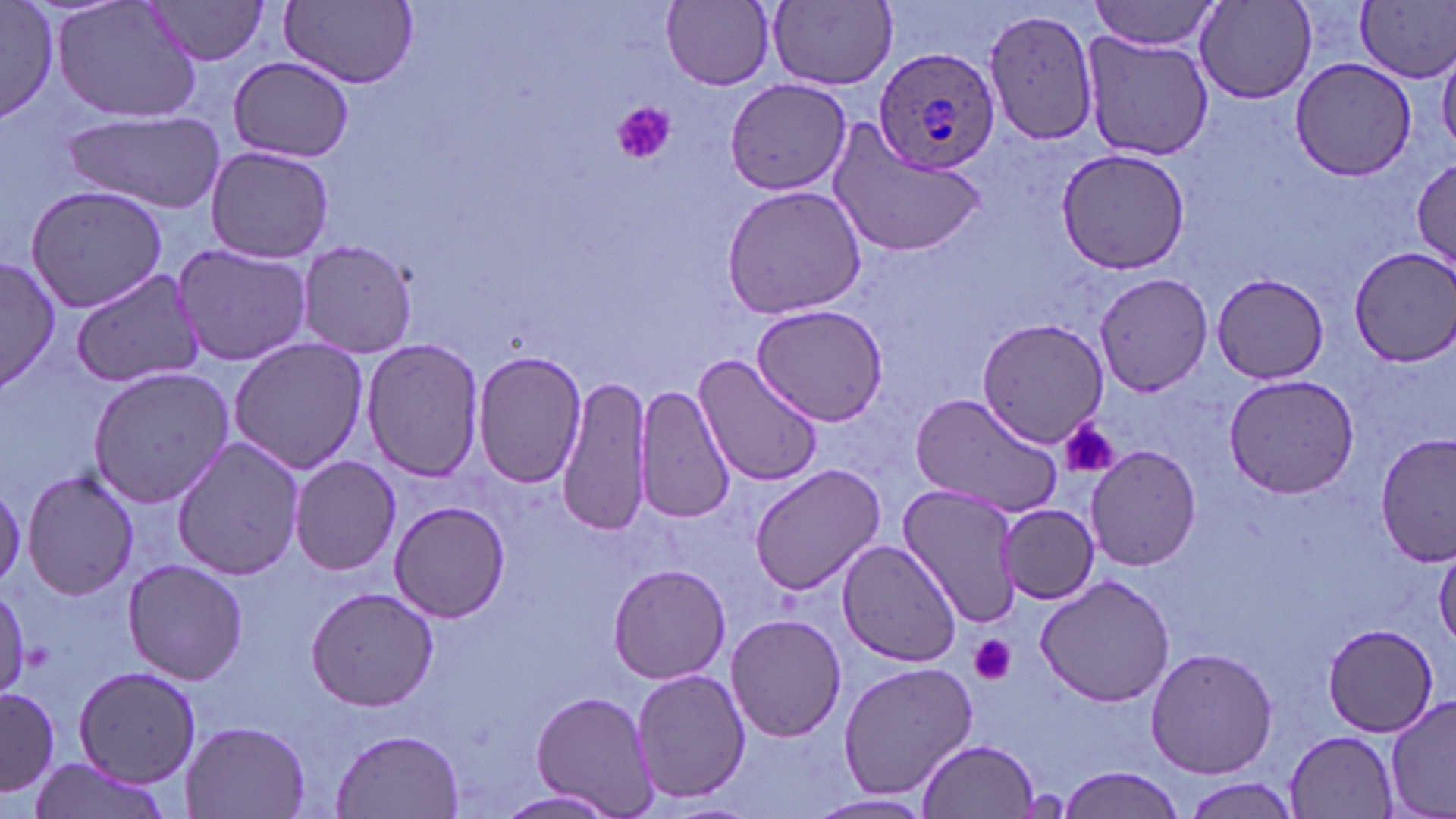 Approximate bounding boxes as (x1,y1)-(x2,y2) corner pairs in pixels. Uninfected red blood cell locations: (0,0)-(63,126), (52,0)-(203,124), (142,0)-(272,66), (282,0)-(418,88), (768,0)-(898,88), (1357,0)-(1455,83), (662,1)-(774,89), (1090,1)-(1220,50), (1196,2)-(1317,104), (984,8)-(1098,147), (1081,29)-(1214,163), (227,56)-(355,162), (1290,58)-(1418,181), (722,78)-(852,196), (63,110)-(227,212), (823,118)-(986,262), (204,144)-(335,263), (1056,149)-(1190,275), (1412,152)-(1455,275), (24,184)-(170,313), (720,184)-(870,320), (294,240)-(417,358), (171,242)-(312,365), (1350,246)-(1456,367), (0,255)-(60,391), (71,268)-(204,387), (1093,271)-(1211,395), (1211,273)-(1329,383), (752,303)-(891,427), (975,318)-(1108,446), (227,336)-(371,473), (361,339)-(484,483), (473,349)-(588,489), (693,353)-(822,487), (85,367)-(235,507), (556,373)-(653,541), (1224,373)-(1361,499), (634,383)-(735,524), (909,391)-(1067,517), (1375,435)-(1454,568), (171,436)-(305,580), (1085,445)-(1201,571), (289,457)-(400,574), (749,462)-(888,596), (23,470)-(142,600), (896,480)-(1023,630), (390,501)-(511,621), (996,504)-(1098,604), (837,539)-(962,666), (1434,542)-(1456,648), (121,559)-(249,684), (607,564)-(731,683), (1033,573)-(1176,705), (0,585)-(34,697), (304,586)-(442,712), (725,612)-(846,742), (1323,624)-(1440,735), (1144,646)-(1279,779), (836,660)-(980,799), (74,665)-(201,787), (631,668)-(749,806), (0,686)-(59,800), (530,689)-(660,815), (1385,696)-(1455,819), (184,719)-(312,819), (328,728)-(465,817), (1284,731)-(1402,818), (921,737)-(1039,818), (23,757)-(174,819), (1058,768)-(1183,819), (1182,778)-(1306,817), (494,788)-(624,818), (804,792)-(938,819). Plasmodium ovale-infected red blood cell locations: (872,44)-(1001,177). Platelet locations: (609,102)-(675,166), (1059,419)-(1119,480), (970,635)-(1017,685). Slide-level diagnosis: Plasmodium ovale. One field of a larger specimen. Optical microscopy. Image is 1456×819 pixels. 1000x magnification. May-Grünwald-Giemsa-stained preparation. Thin blood film.